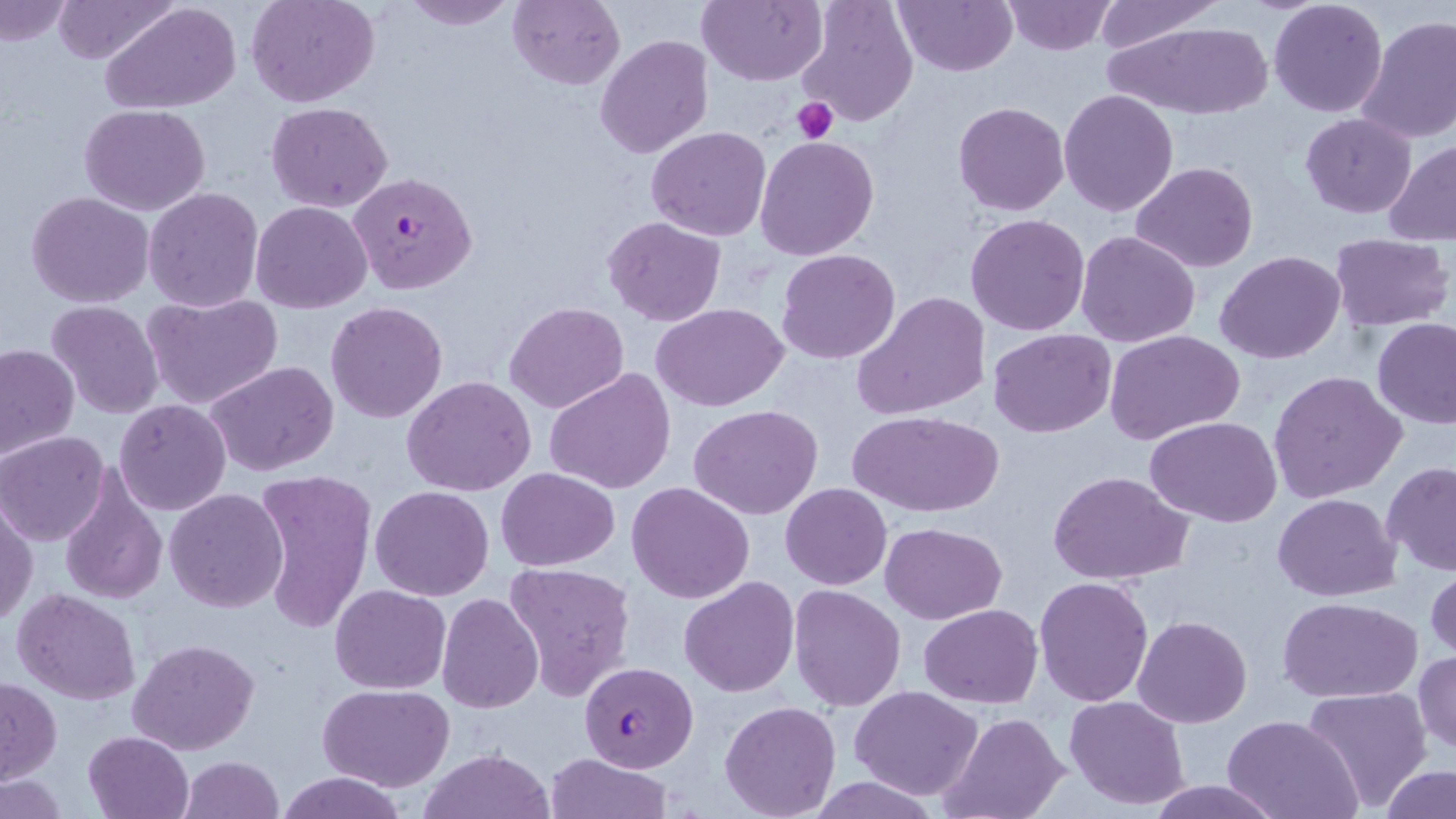
Summary:
  - Coordinate format: approximate bounding boxes as (x1,y1)-(x2,y2) corner pairs in pixels
  - Uninfected red blood cell locations: (52,0)-(182,67), (247,0)-(381,107), (400,0)-(518,29), (507,0)-(625,90), (697,0)-(824,86), (892,0)-(1018,77), (1087,0)-(1226,48), (1,1)-(73,45), (102,1)-(243,113), (1001,1)-(1117,54), (1267,1)-(1389,118), (796,3)-(918,129), (1355,14)-(1456,145), (1106,21)-(1274,121), (595,34)-(714,157), (1059,89)-(1180,216), (267,101)-(393,212), (954,101)-(1070,217), (79,103)-(211,215), (1300,113)-(1418,219), (647,127)-(770,242), (754,134)-(881,261), (1383,142)-(1456,247), (1130,161)-(1259,273), (143,187)-(265,312), (27,191)-(155,309), (251,201)-(373,314), (965,213)-(1090,337), (602,215)-(726,326), (1076,230)-(1200,347), (1329,234)-(1453,330), (776,248)-(902,364), (1216,250)-(1347,364), (783,262)-(982,395), (853,291)-(991,421), (142,292)-(283,411), (46,300)-(163,420), (325,301)-(449,423), (504,301)-(629,413), (651,303)-(790,412), (1373,319)-(1456,429), (987,328)-(1116,438), (1105,328)-(1246,444), (1,342)-(79,462), (206,360)-(337,475), (545,369)-(677,495), (1269,371)-(1406,501), (402,376)-(536,497), (114,400)-(230,515), (688,404)-(823,519), (850,410)-(1004,518), (1146,417)-(1281,527), (1,431)-(113,546), (1382,463)-(1455,577), (59,467)-(168,606), (495,467)-(620,570), (254,469)-(376,633), (1048,470)-(1193,585), (627,481)-(755,603), (781,483)-(892,589), (370,485)-(495,600), (164,488)-(289,612), (1272,493)-(1399,602), (1,499)-(38,625), (880,522)-(1007,624), (504,561)-(637,701), (1426,563)-(1456,665), (1034,574)-(1153,707), (678,577)-(800,697), (331,584)-(450,694), (788,584)-(907,712), (12,589)-(140,705), (436,592)-(543,713), (1276,596)-(1424,704), (918,605)-(1041,707), (1133,614)-(1253,727), (127,638)-(258,754), (1413,652)-(1455,756), (1,676)-(62,784), (318,684)-(454,791), (850,684)-(985,800), (1302,685)-(1433,810), (1064,695)-(1191,810), (719,701)-(841,818), (941,712)-(1069,819), (1223,715)-(1362,819), (83,730)-(194,819), (419,749)-(555,819), (545,753)-(675,818), (178,755)-(285,818), (1380,764)-(1455,819), (277,771)-(408,819), (0,776)-(69,818), (1145,780)-(1281,818)
  - Plasmodium falciparum-infected red blood cell locations: (350,172)-(478,294), (578,660)-(699,772)
  - Platelet locations: (790,97)-(839,145)
  - Slide-level diagnosis: Plasmodium falciparum
  - Magnification: 1000x
  - Stain: May-Grünwald-Giemsa
  - Modality: optical microscopy
  - Image size: 1456×819 pixels
  - Preparation: thin blood smear
  - Field of view: single